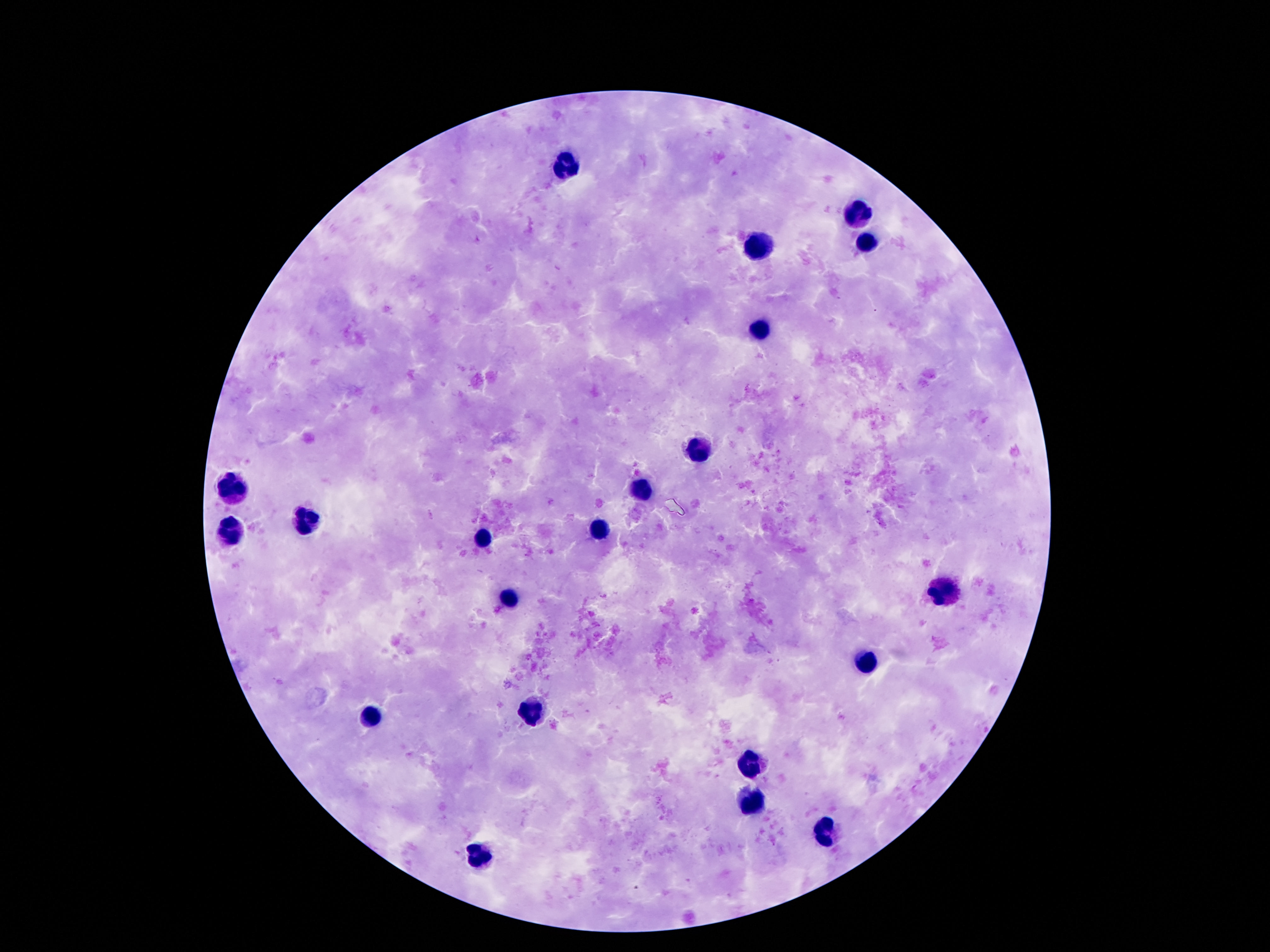

Approximate object centers, in pixels from the top-left corner. Leukocyte locations: (x=567, y=162), (x=856, y=215), (x=866, y=243), (x=754, y=245), (x=759, y=331), (x=698, y=450), (x=235, y=491), (x=640, y=491), (x=308, y=519), (x=231, y=530), (x=599, y=534), (x=478, y=536), (x=942, y=589), (x=506, y=599), (x=866, y=663), (x=532, y=709), (x=371, y=714), (x=750, y=765), (x=748, y=797), (x=821, y=833), (x=478, y=855). Single field of view. Patient malaria status: negative. Thick blood film. Giemsa stain. 100x magnification. Image is 1270×952 pixels. Smartphone photograph taken through the microscope eyepiece.